Give a bounding box for every Plasmodium parasite, every leukocyte, and every artifact (stain precipitate or debris).
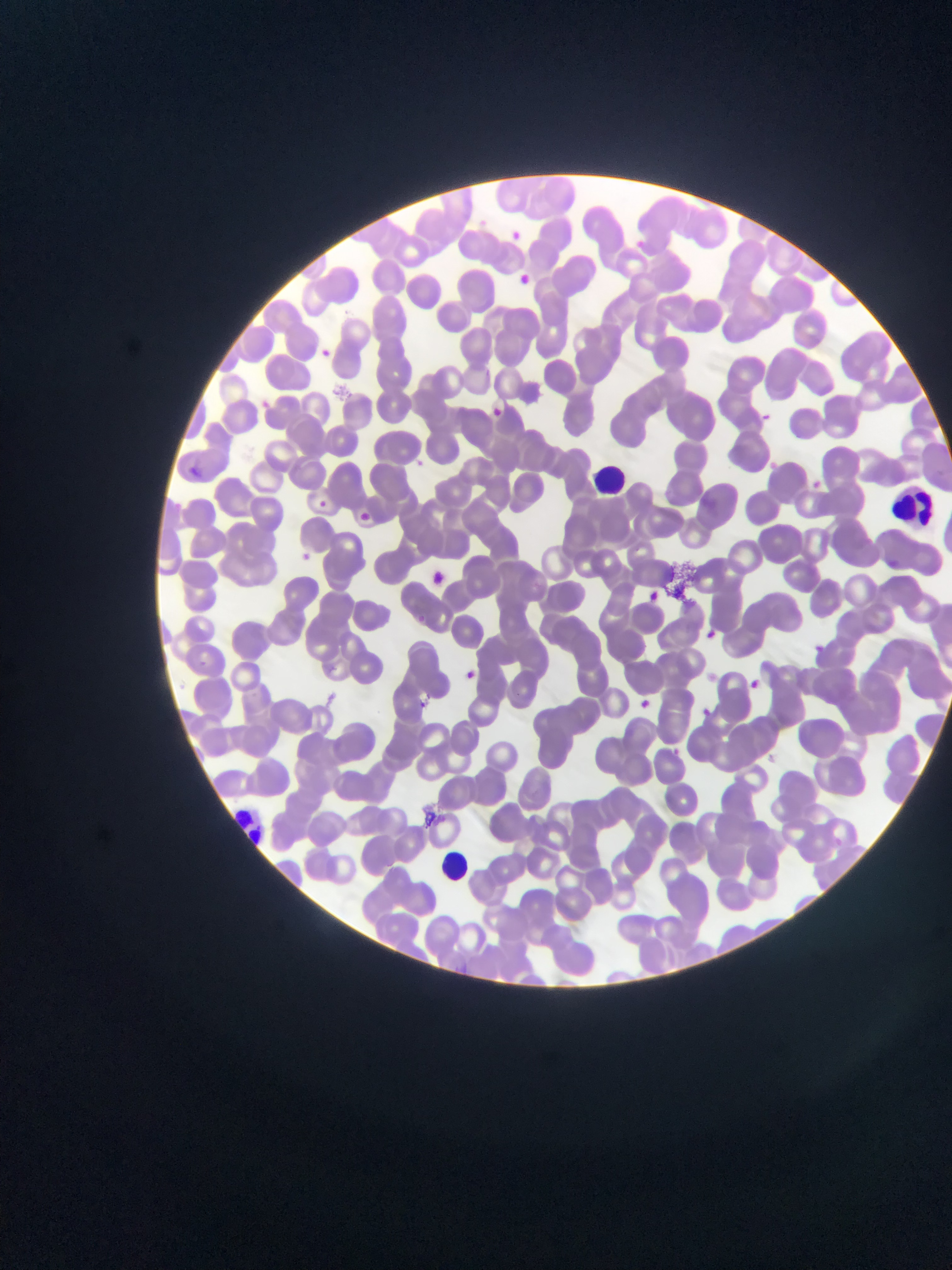
Approximate bounding boxes as (left, top, right, bottom) in pixels.
Plasmodium parasites: (505, 226, 526, 246), (511, 271, 535, 293), (315, 344, 335, 363), (482, 403, 506, 423), (753, 412, 776, 433), (416, 457, 430, 466), (183, 461, 201, 474), (808, 477, 825, 492), (315, 498, 330, 512), (355, 510, 372, 524), (297, 548, 315, 565), (425, 568, 451, 590), (641, 588, 662, 607), (704, 623, 721, 640), (811, 643, 825, 657), (459, 667, 481, 686), (746, 677, 761, 692), (415, 696, 434, 715), (635, 696, 653, 713), (698, 706, 713, 721), (667, 745, 684, 760).
Leukocytes: (587, 460, 635, 493), (886, 481, 937, 536), (223, 803, 266, 851), (436, 847, 469, 878).
Artifacts (stain precipitate or debris): (666, 560, 705, 599).

Thin blood smear. Mobile-phone photograph taken through the microscope. Image is 952×1270 pixels. One field of view. Collected in Ghana.